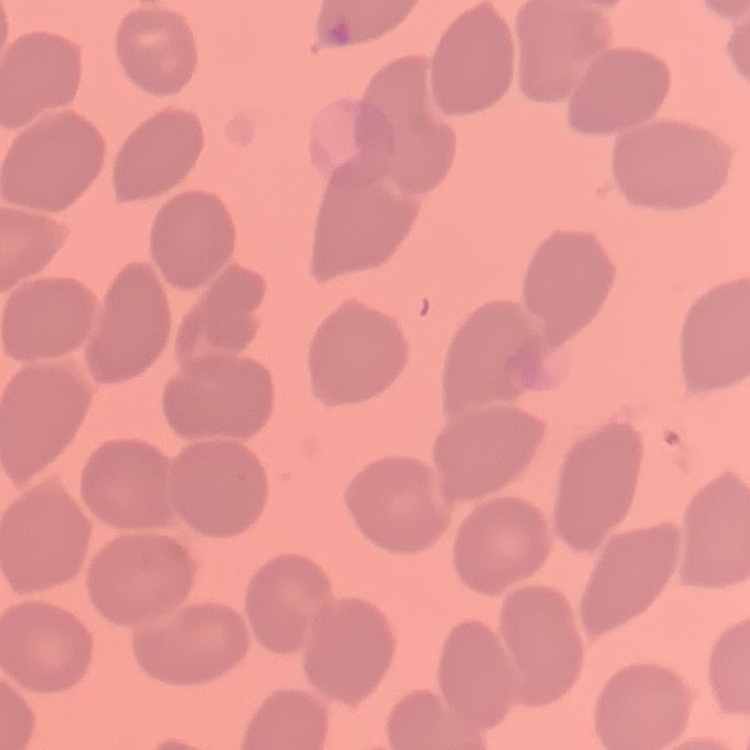

The red blood cells exhibit no rouleaux formation. One tile cut from a larger photomicrograph. Stained with either Field's or Giemsa. Thin peripheral smear.